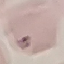
result = negative for malaria parasites
stain = Giemsa
image type = automatically extracted cell patch, resized to 64 × 64 pixels
capture = smartphone camera at the microscope eyepiece
preparation = thin blood film